Outline each Plasmodium ovale-infected red blood cell.
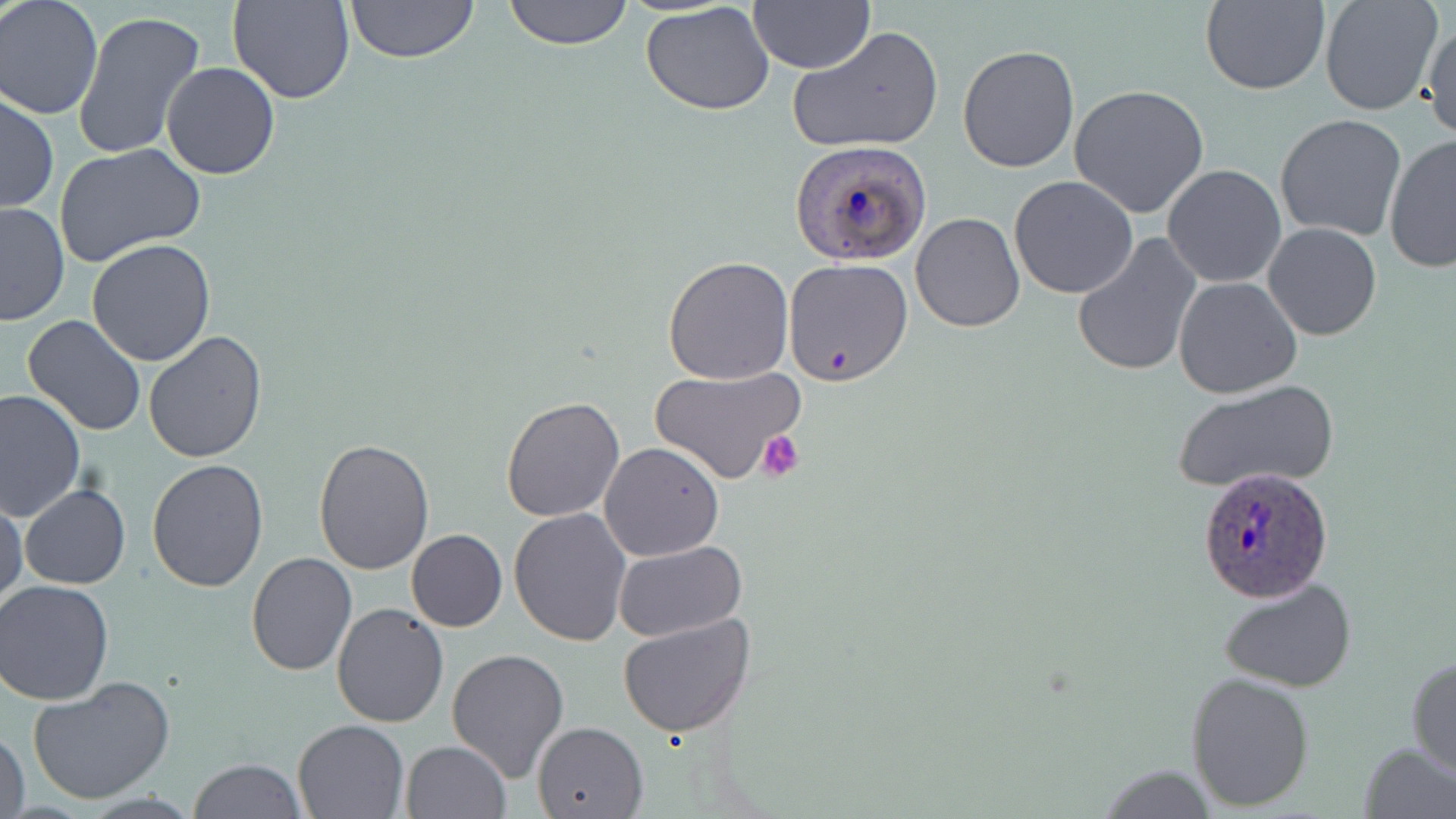
Approximate bounding boxes as named x1/y1/x2/y2 corners in pixels.
Plasmodium ovale-infected red blood cells: (x1=791, y1=141, x2=933, y2=265), (x1=1195, y1=465, x2=1335, y2=603).

Platelet locations: (x1=756, y1=432, x2=802, y2=482). Uninfected red blood cell locations: (x1=228, y1=0, x2=355, y2=105), (x1=342, y1=0, x2=482, y2=64), (x1=502, y1=0, x2=635, y2=49), (x1=1199, y1=0, x2=1330, y2=95), (x1=1319, y1=0, x2=1442, y2=117), (x1=0, y1=1, x2=103, y2=119), (x1=749, y1=1, x2=872, y2=75), (x1=641, y1=2, x2=776, y2=117), (x1=73, y1=11, x2=207, y2=163), (x1=1422, y1=13, x2=1456, y2=144), (x1=790, y1=26, x2=944, y2=154), (x1=956, y1=44, x2=1080, y2=175), (x1=161, y1=61, x2=279, y2=180), (x1=1068, y1=83, x2=1211, y2=218), (x1=0, y1=92, x2=58, y2=215), (x1=1275, y1=114, x2=1408, y2=242), (x1=1384, y1=132, x2=1455, y2=273), (x1=54, y1=143, x2=206, y2=268), (x1=1161, y1=164, x2=1286, y2=288), (x1=1009, y1=176, x2=1139, y2=299), (x1=0, y1=200, x2=71, y2=325), (x1=910, y1=212, x2=1026, y2=332), (x1=1263, y1=223, x2=1382, y2=341), (x1=1070, y1=232, x2=1203, y2=379), (x1=86, y1=239, x2=217, y2=367), (x1=662, y1=256, x2=794, y2=385), (x1=784, y1=260, x2=913, y2=387), (x1=1172, y1=276, x2=1302, y2=399), (x1=22, y1=315, x2=147, y2=438), (x1=143, y1=331, x2=269, y2=464), (x1=649, y1=365, x2=805, y2=485), (x1=1171, y1=379, x2=1339, y2=494), (x1=0, y1=389, x2=85, y2=523), (x1=500, y1=395, x2=625, y2=522), (x1=312, y1=440, x2=436, y2=574), (x1=598, y1=441, x2=725, y2=562), (x1=146, y1=459, x2=268, y2=592), (x1=20, y1=484, x2=130, y2=589), (x1=1, y1=495, x2=26, y2=608), (x1=508, y1=509, x2=633, y2=647), (x1=405, y1=529, x2=507, y2=632), (x1=614, y1=541, x2=746, y2=640), (x1=246, y1=554, x2=357, y2=676), (x1=1218, y1=575, x2=1356, y2=693), (x1=1, y1=579, x2=118, y2=704), (x1=332, y1=603, x2=449, y2=728), (x1=617, y1=614, x2=756, y2=738), (x1=445, y1=646, x2=570, y2=781), (x1=1406, y1=654, x2=1455, y2=778), (x1=1185, y1=670, x2=1316, y2=811), (x1=26, y1=677, x2=176, y2=806), (x1=292, y1=718, x2=411, y2=818), (x1=532, y1=721, x2=648, y2=818), (x1=1, y1=726, x2=29, y2=819), (x1=401, y1=740, x2=511, y2=819), (x1=1359, y1=741, x2=1456, y2=818), (x1=188, y1=758, x2=308, y2=818), (x1=1092, y1=764, x2=1220, y2=816). Slide-level diagnosis: Plasmodium ovale. Single field of view. Thin blood smear. Image is 1456×819 pixels. 1000x magnification. May-Grünwald-Giemsa-stained preparation. Light microscopy.